Classify this cell by malaria status.
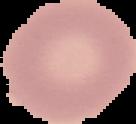

Uninfected.

Cell region segmented out of the field of view; the surrounding area is masked to black. Image is 136×124 pixels. From a thin blood film.